Report the malaria status of this cell.
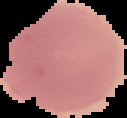

It is uninfected.

The area outside the segmented cell region is set to black. Image is 127×118 pixels. From a thin blood film.